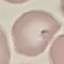
result = malaria parasites identified
preparation = thin blood film
capture = smartphone camera at the microscope eyepiece
image type = cell patch, automatically extracted from a larger field of view and resized to 64 × 64 pixels
stain = Giemsa